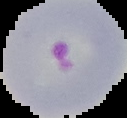

preparation: thin blood smear
malaria_status: parasitized
image_size: 127×118 pixels
image_type: cell region segmented out of the field of view; surrounding area masked to black